Give the position of every Plasmodium parasite.
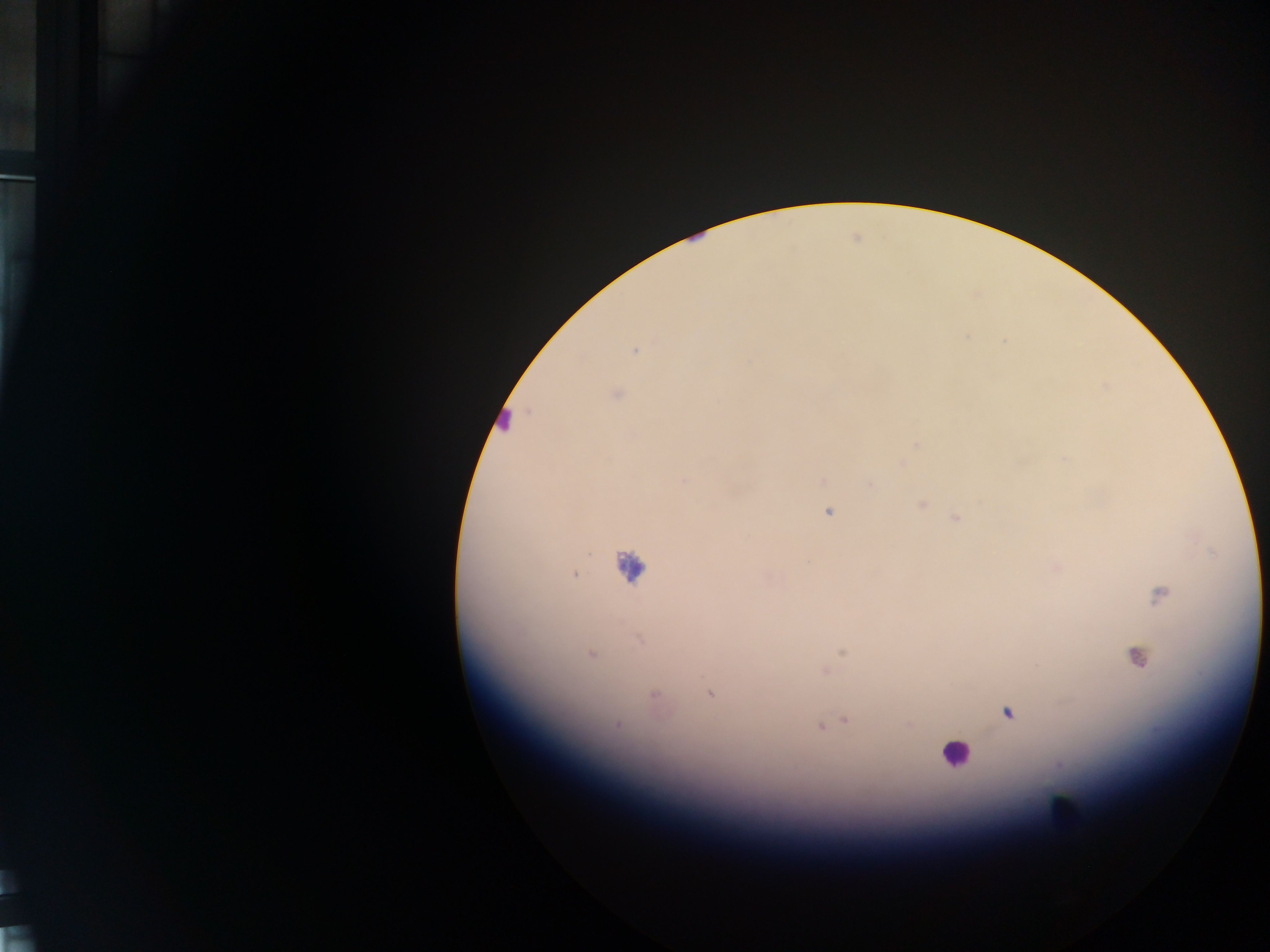
Approximate centers as (x, y) in pixels.
Plasmodium parasites: (636, 351), (614, 393), (915, 445), (1064, 457), (684, 480), (821, 481), (870, 484), (921, 503), (828, 512), (957, 519), (1056, 567), (574, 575), (1158, 595), (639, 640), (842, 652), (590, 655), (1136, 658), (824, 671), (709, 693), (654, 696), (1008, 713), (845, 720), (827, 724), (908, 724), (616, 725), (820, 725).

Summary:
  - Leukocyte locations: (505, 420), (628, 566), (954, 753), (1065, 809)
  - Capture: mobile-phone photograph through a microscope
  - Field of view: single
  - Country: Ghana
  - Preparation: thick blood smear
  - Image size: 1270×952 pixels